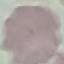 Result: no malaria parasites detected. Giemsa-stained preparation. Acquired by smartphone through the microscope eyepiece. Automatically extracted cell patch, resized to 64 × 64 pixels. Thin blood smear.